Describe the morphology of the erythrocytes.
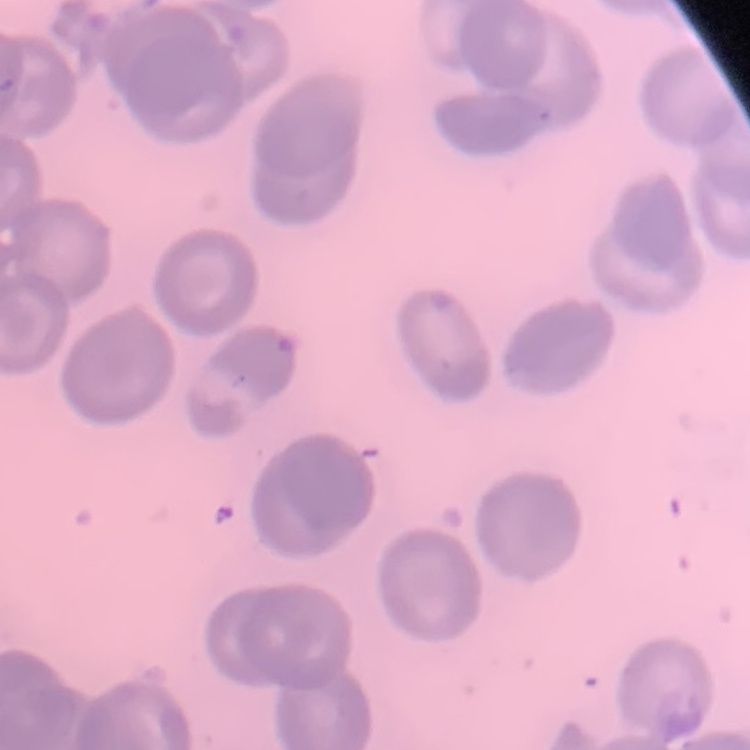

No rouleaux formation.

Summary:
  - Stain: Field's or Giemsa
  - Preparation: thin blood smear
  - Image type: square crop of a larger photomicrograph